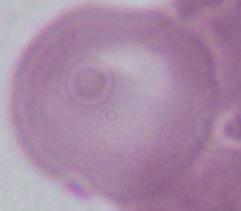

modality: photomicrograph
magnification: 1000x
identification: red blood cell